Name the cell type shown.
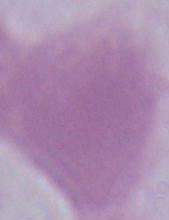

This is an erythrocyte.

modality = photomicrograph
magnification = 1000x